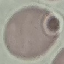

Summary:
  - Malaria status: uninfected
  - Stain: Giemsa
  - Image type: cell patch, automatically extracted from a larger field of view and resized to 64 × 64 pixels
  - Preparation: thin smear
  - Capture: smartphone camera at the microscope eyepiece